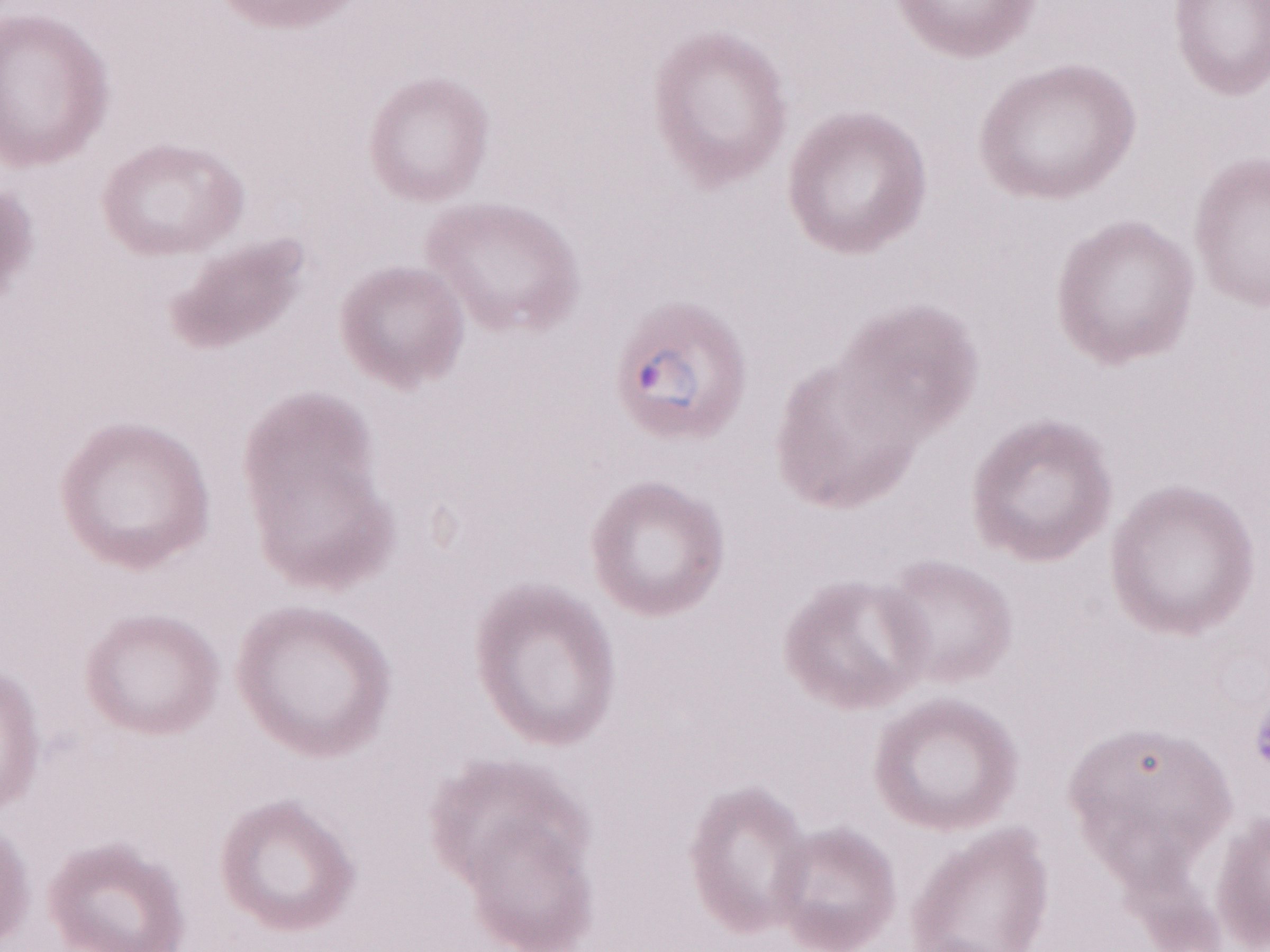

Patient-level malaria diagnosis: positive. Magnification: 1,000x. May-Grünwald-Giemsa-stained preparation. Olympus BX43 microscope, Olympus DP73 camera. Image is 1270×952 pixels. Single field of view. Thin peripheral-blood smear.